Locate and identify every blood parasite.
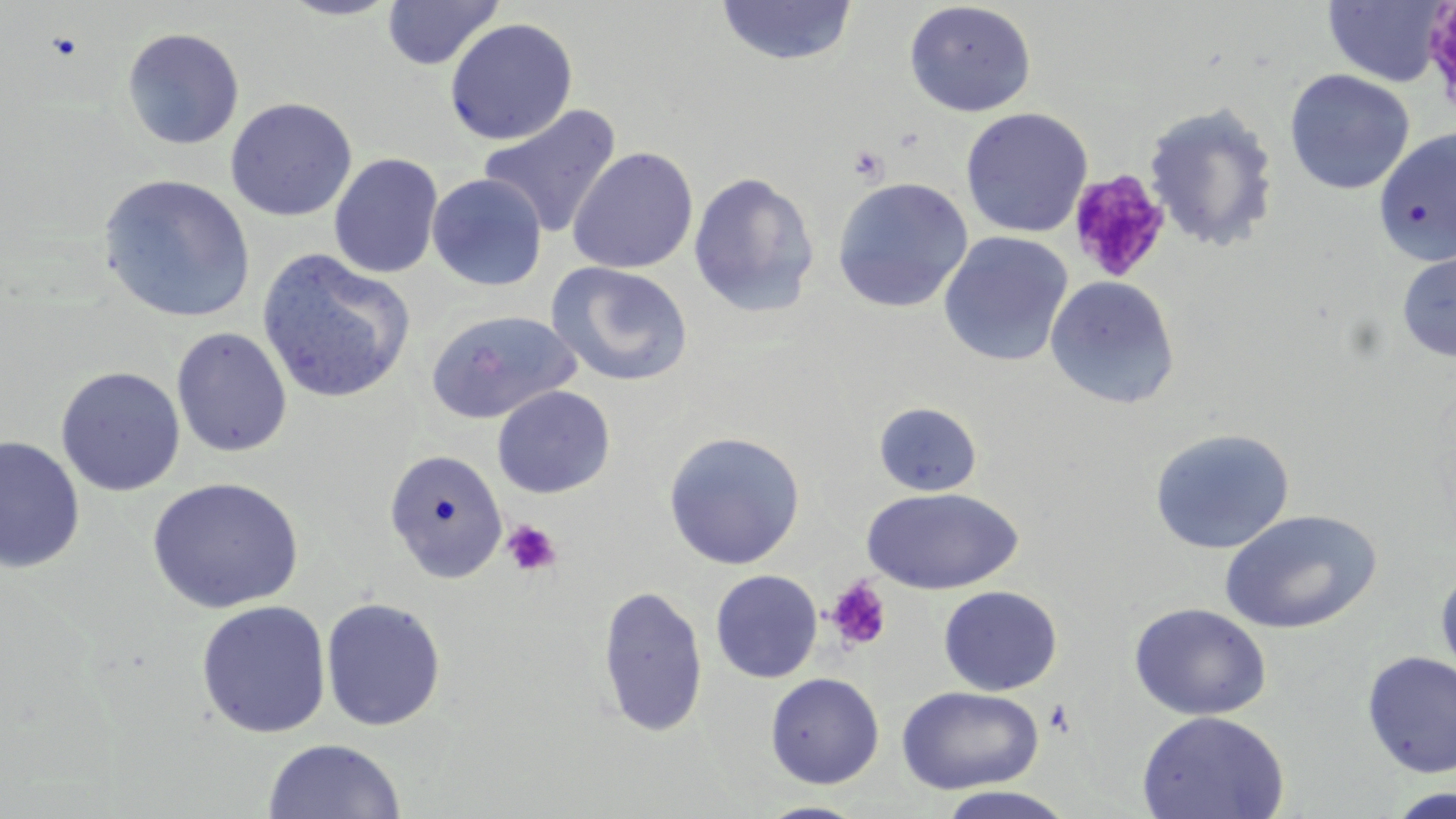

No blood parasites observed.

Approximate bounding boxes as named x1/y1/x2/y2 corners in pixels. Platelet locations: (x1=1423, y1=4, x2=1456, y2=116), (x1=848, y1=144, x2=889, y2=184), (x1=1066, y1=170, x2=1172, y2=283), (x1=501, y1=520, x2=562, y2=578), (x1=825, y1=578, x2=892, y2=652). Uninfected red blood cell locations: (x1=276, y1=0, x2=404, y2=21), (x1=381, y1=0, x2=504, y2=71), (x1=1322, y1=0, x2=1450, y2=87), (x1=715, y1=1, x2=858, y2=67), (x1=904, y1=1, x2=1036, y2=117), (x1=444, y1=17, x2=579, y2=145), (x1=121, y1=27, x2=244, y2=150), (x1=1284, y1=69, x2=1415, y2=195), (x1=225, y1=97, x2=357, y2=222), (x1=1143, y1=102, x2=1280, y2=253), (x1=477, y1=103, x2=622, y2=239), (x1=961, y1=107, x2=1093, y2=238), (x1=1374, y1=130, x2=1455, y2=265), (x1=567, y1=146, x2=699, y2=274), (x1=329, y1=152, x2=444, y2=279), (x1=688, y1=171, x2=820, y2=317), (x1=426, y1=173, x2=548, y2=291), (x1=98, y1=174, x2=256, y2=323), (x1=832, y1=177, x2=973, y2=313), (x1=938, y1=231, x2=1073, y2=367), (x1=256, y1=248, x2=416, y2=404), (x1=1396, y1=248, x2=1456, y2=362), (x1=547, y1=261, x2=693, y2=388), (x1=1045, y1=276, x2=1181, y2=409), (x1=424, y1=309, x2=582, y2=425), (x1=171, y1=327, x2=292, y2=458), (x1=55, y1=366, x2=186, y2=497), (x1=491, y1=385, x2=616, y2=498), (x1=873, y1=402, x2=982, y2=497), (x1=1149, y1=427, x2=1296, y2=555), (x1=662, y1=430, x2=805, y2=569), (x1=0, y1=435, x2=85, y2=574), (x1=383, y1=449, x2=508, y2=583), (x1=147, y1=477, x2=304, y2=614), (x1=861, y1=487, x2=1023, y2=595), (x1=1219, y1=509, x2=1382, y2=634), (x1=1435, y1=563, x2=1456, y2=688), (x1=710, y1=569, x2=823, y2=683), (x1=596, y1=584, x2=708, y2=738), (x1=938, y1=585, x2=1062, y2=696), (x1=320, y1=596, x2=447, y2=732), (x1=196, y1=600, x2=332, y2=739), (x1=1129, y1=603, x2=1271, y2=720), (x1=1361, y1=651, x2=1456, y2=778), (x1=765, y1=672, x2=884, y2=788), (x1=896, y1=686, x2=1045, y2=795), (x1=1137, y1=710, x2=1290, y2=819), (x1=261, y1=738, x2=405, y2=819), (x1=934, y1=786, x2=1079, y2=818), (x1=1384, y1=787, x2=1456, y2=818), (x1=753, y1=801, x2=871, y2=819). Slide-level diagnosis: negative for blood parasites. One field of a larger specimen. Light microscopy. Image is 1456×819 pixels. May-Grünwald-Giemsa-stained preparation. Thin blood smear. Captured at 1000x magnification.